Locate every Plasmodium falciparum-infected red blood cell.
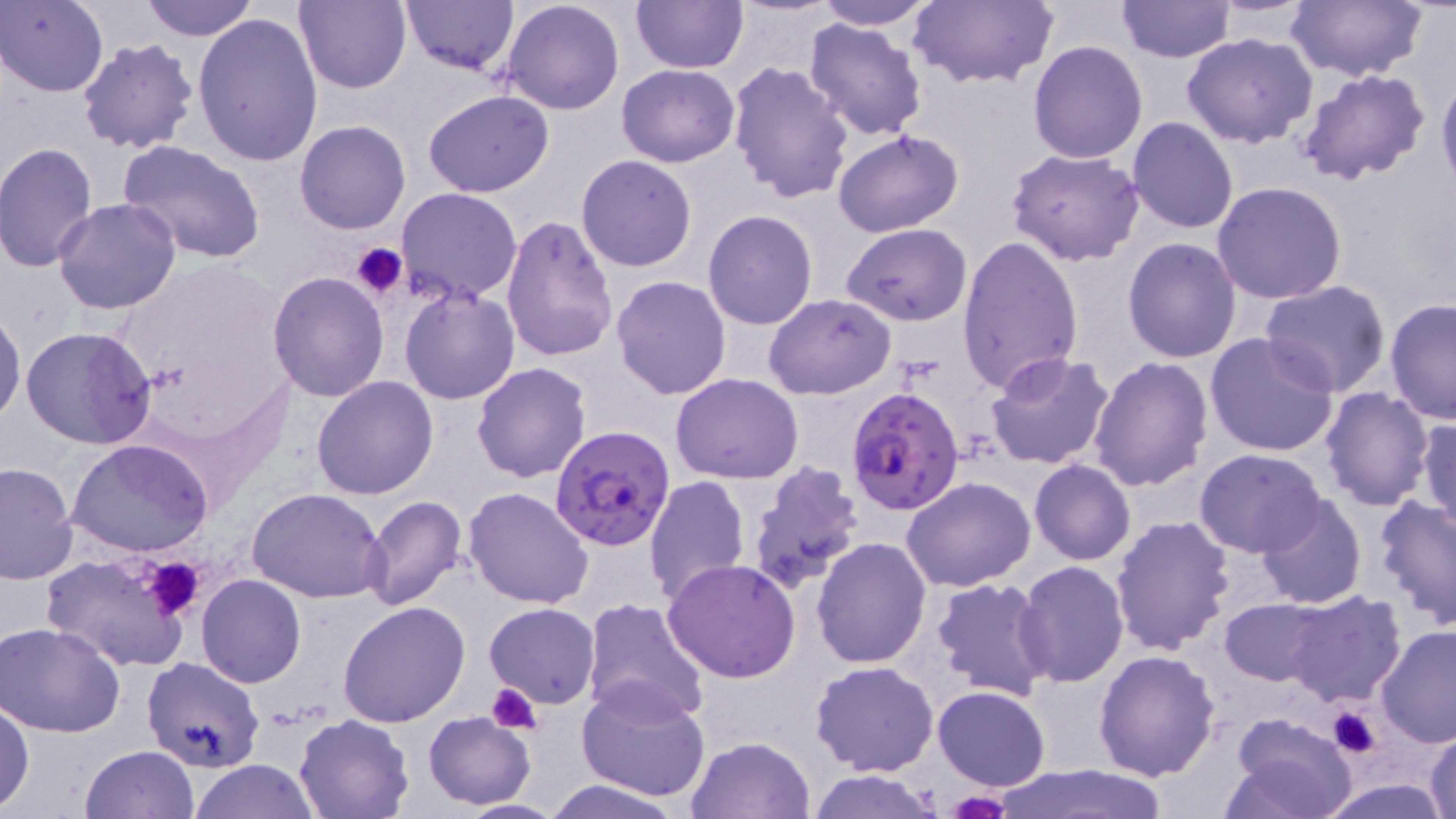
Approximate bounding boxes as named x1/y1/x2/y2 corners in pixels.
Plasmodium falciparum-infected red blood cells: (x1=844, y1=385, x2=967, y2=516), (x1=548, y1=425, x2=676, y2=552).

Summary:
  - Platelet locations: (x1=348, y1=241, x2=407, y2=300), (x1=135, y1=554, x2=207, y2=621), (x1=486, y1=681, x2=542, y2=735), (x1=1328, y1=707, x2=1382, y2=758), (x1=944, y1=792, x2=1011, y2=819)
  - Uninfected red blood cell locations: (x1=140, y1=0, x2=256, y2=41), (x1=295, y1=0, x2=412, y2=94), (x1=399, y1=0, x2=519, y2=74), (x1=631, y1=0, x2=746, y2=72), (x1=814, y1=0, x2=940, y2=29), (x1=905, y1=0, x2=1059, y2=90), (x1=1115, y1=0, x2=1235, y2=64), (x1=1287, y1=0, x2=1426, y2=81), (x1=2, y1=1, x2=108, y2=96), (x1=500, y1=1, x2=626, y2=116), (x1=193, y1=11, x2=325, y2=168), (x1=803, y1=18, x2=927, y2=140), (x1=1182, y1=33, x2=1317, y2=148), (x1=77, y1=37, x2=199, y2=154), (x1=1027, y1=41, x2=1148, y2=163), (x1=727, y1=61, x2=855, y2=203), (x1=617, y1=63, x2=738, y2=166), (x1=1298, y1=68, x2=1430, y2=187), (x1=1437, y1=69, x2=1456, y2=197), (x1=424, y1=91, x2=553, y2=198), (x1=1126, y1=116, x2=1239, y2=234), (x1=295, y1=120, x2=412, y2=235), (x1=832, y1=129, x2=964, y2=238), (x1=117, y1=139, x2=266, y2=263), (x1=1, y1=142, x2=99, y2=272), (x1=1007, y1=146, x2=1147, y2=266), (x1=576, y1=155, x2=699, y2=272), (x1=1212, y1=181, x2=1347, y2=302), (x1=395, y1=188, x2=524, y2=304), (x1=53, y1=197, x2=183, y2=316), (x1=702, y1=210, x2=817, y2=329), (x1=501, y1=213, x2=619, y2=363), (x1=841, y1=224, x2=971, y2=327), (x1=958, y1=234, x2=1085, y2=396), (x1=1122, y1=237, x2=1241, y2=363), (x1=268, y1=272, x2=389, y2=402), (x1=610, y1=275, x2=732, y2=399), (x1=1259, y1=280, x2=1392, y2=395), (x1=398, y1=283, x2=522, y2=405), (x1=764, y1=294, x2=895, y2=399), (x1=1384, y1=298, x2=1456, y2=423), (x1=0, y1=308, x2=25, y2=430), (x1=21, y1=325, x2=156, y2=450), (x1=1204, y1=332, x2=1340, y2=459), (x1=986, y1=352, x2=1114, y2=470), (x1=1088, y1=356, x2=1213, y2=492), (x1=471, y1=362, x2=593, y2=483), (x1=670, y1=373, x2=804, y2=485), (x1=311, y1=376, x2=438, y2=499), (x1=1319, y1=386, x2=1435, y2=513), (x1=1417, y1=415, x2=1455, y2=536), (x1=66, y1=437, x2=212, y2=556), (x1=1194, y1=448, x2=1327, y2=559), (x1=1029, y1=459, x2=1136, y2=566), (x1=0, y1=460, x2=77, y2=584), (x1=747, y1=464, x2=868, y2=595), (x1=644, y1=475, x2=751, y2=607), (x1=902, y1=476, x2=1036, y2=591), (x1=464, y1=486, x2=595, y2=608), (x1=247, y1=489, x2=388, y2=604), (x1=1253, y1=492, x2=1368, y2=610), (x1=1372, y1=494, x2=1456, y2=627), (x1=359, y1=496, x2=469, y2=611), (x1=1109, y1=513, x2=1235, y2=657), (x1=811, y1=536, x2=931, y2=667), (x1=42, y1=553, x2=195, y2=671), (x1=662, y1=559, x2=803, y2=683), (x1=1015, y1=563, x2=1129, y2=688), (x1=196, y1=575, x2=306, y2=688), (x1=930, y1=576, x2=1054, y2=702), (x1=1283, y1=591, x2=1407, y2=706), (x1=582, y1=597, x2=711, y2=722), (x1=1220, y1=598, x2=1327, y2=685), (x1=337, y1=600, x2=471, y2=727), (x1=484, y1=603, x2=600, y2=710), (x1=0, y1=621, x2=127, y2=737), (x1=1374, y1=625, x2=1456, y2=747), (x1=1093, y1=649, x2=1221, y2=779), (x1=141, y1=655, x2=264, y2=772), (x1=810, y1=660, x2=939, y2=776), (x1=577, y1=682, x2=711, y2=803), (x1=934, y1=686, x2=1051, y2=790), (x1=0, y1=700, x2=34, y2=814), (x1=423, y1=712, x2=536, y2=810), (x1=1226, y1=712, x2=1356, y2=818), (x1=295, y1=713, x2=416, y2=818), (x1=1426, y1=728, x2=1456, y2=819), (x1=685, y1=735, x2=814, y2=818), (x1=80, y1=744, x2=198, y2=819), (x1=190, y1=759, x2=319, y2=818), (x1=992, y1=763, x2=1172, y2=818), (x1=809, y1=769, x2=942, y2=819), (x1=538, y1=778, x2=689, y2=818), (x1=1314, y1=778, x2=1452, y2=818), (x1=446, y1=798, x2=571, y2=818)
  - Slide-level diagnosis: Plasmodium falciparum
  - Preparation: thin blood film
  - Field of view: one of a larger specimen
  - Image size: 1456×819 pixels
  - Magnification: 1000x
  - Stain: May-Grünwald-Giemsa
  - Modality: optical microscopy